Name the cell type shown.
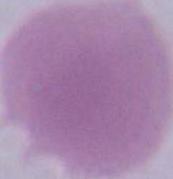
An erythrocyte.

modality = micrograph
magnification = 1000x